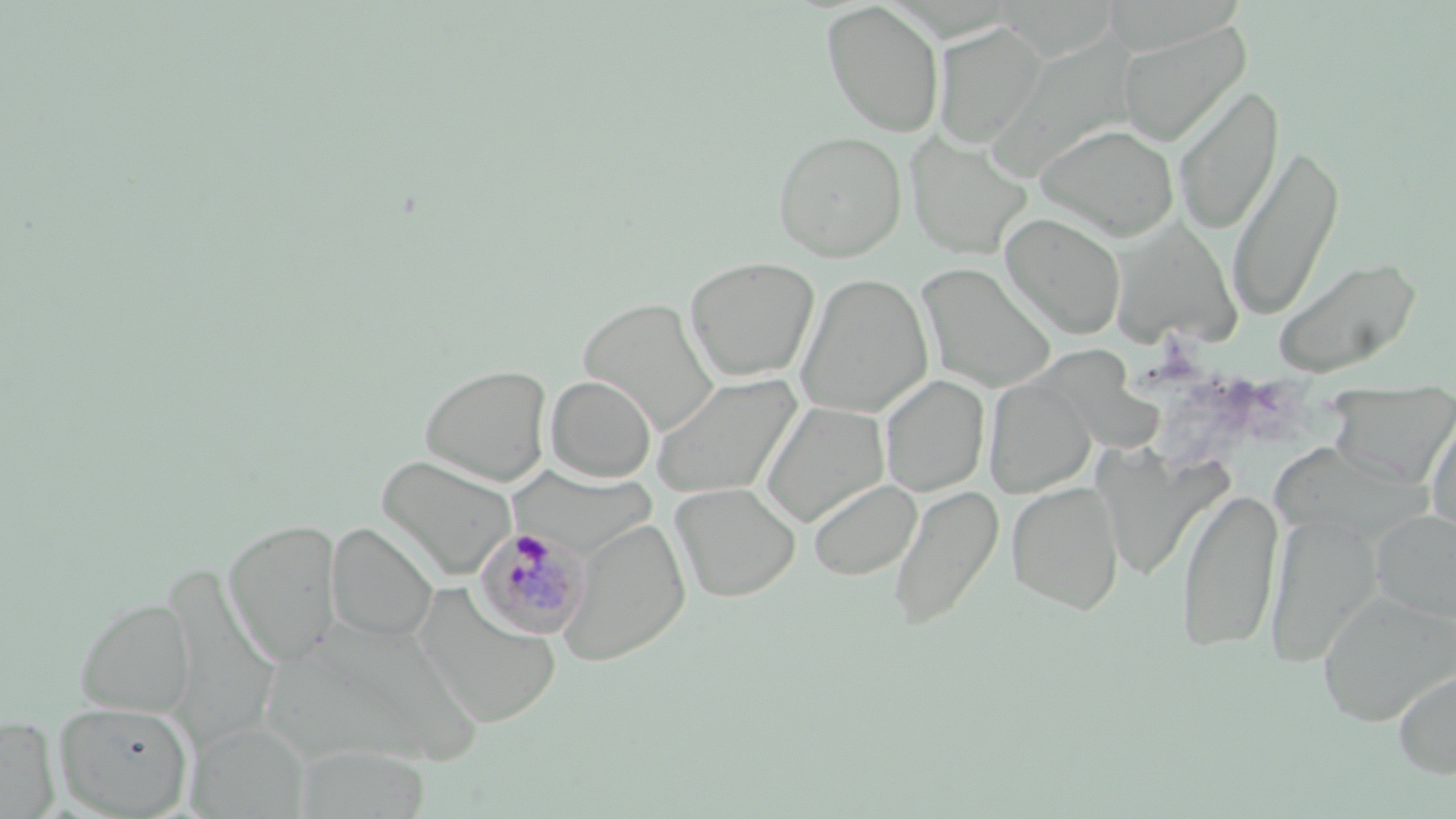
slide_level_diagnosis: Plasmodium malariae
field_of_view: single
plasmodium_malariae_infected_red_blood_cell_locations: 'approximate bounding boxes as (x1,y1)-(x2,y2) corner pairs in pixels: (473,525)-(591,641)'
modality: light microscopy
stain: May-Grünwald-Giemsa
preparation: thin blood film
uninfected_red_blood_cell_locations: 'approximate bounding boxes as (x1,y1)-(x2,y2) corner pairs in pixels: (821,1)-(945,138), (933,22)-(1046,148), (1118,22)-(1251,147), (973,35)-(1142,194), (1173,82)-(1284,236), (1035,123)-(1179,240), (772,129)-(907,261), (905,132)-(1034,260), (1227,142)-(1345,322), (1001,212)-(1127,339), (1108,217)-(1242,349), (1272,255)-(1421,379), (684,257)-(819,382), (915,263)-(1058,393), (795,272)-(933,418), (577,297)-(720,436), (1024,338)-(1169,451), (419,363)-(552,486), (650,373)-(802,500), (546,375)-(656,482), (879,375)-(990,497), (984,376)-(1096,497), (758,401)-(890,528), (1425,408)-(1456,539), (1093,446)-(1218,583), (377,455)-(517,580), (807,479)-(923,582), (670,482)-(801,602), (1006,482)-(1125,615), (888,483)-(1003,632), (1176,486)-(1283,654), (1370,510)-(1456,623), (1264,512)-(1380,668), (559,517)-(690,666), (222,519)-(342,668), (327,522)-(438,643), (413,586)-(562,729), (1317,590)-(1456,727), (74,597)-(195,718), (1392,663)-(1456,781), (54,700)-(194,817), (0,715)-(60,818), (187,721)-(309,817), (292,744)-(431,818)'
image_size: 1456×819 pixels
magnification: 1000x